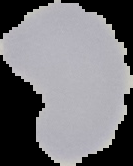
Image is 133×166 pixels. The area outside the segmented cell region is set to black. From a thin blood smear. Malaria status: uninfected.